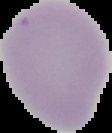 From a thin blood smear. Segmented cell region on a black background. Malaria status: uninfected. Image is 112×133 pixels.